Give the position of each P. falciparum parasite with its life-cycle stage, each leukocyte, and any debris.
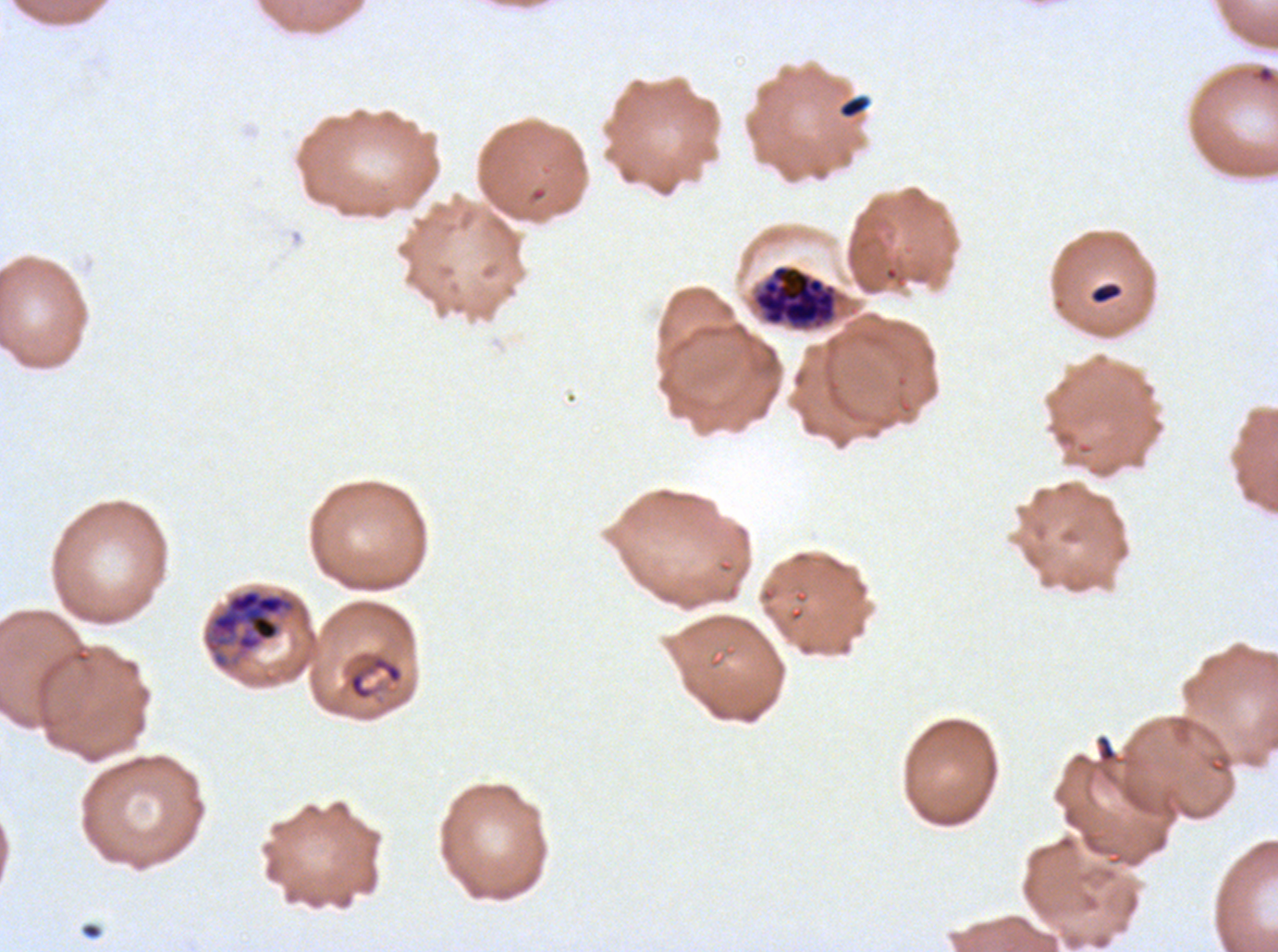

Approximate bounding boxes as {x1, y1, x2, y2} in pixels.
Rings: {1251, 64, 1277, 86}.
Late schizonts: {753, 264, 837, 328}, {203, 588, 300, 671}.
Debris: {837, 93, 872, 120}, {1089, 281, 1123, 305}, {347, 654, 403, 701}.
No late-ring/early-trophozoite forms, mid trophozoites, late trophozoites, early schizonts, segmenters, gametocytes, or leukocytes observed.

Image is 1278×952 pixels. Ex-vivo P. falciparum culture from a patient in The Gambia, grown for 24 to 48 hours. A sub-image separated from a larger composite. Life-cycle stages observed: ring, late schizont. Giemsa stain. Thin blood smear.